Report the malaria status of this cell.
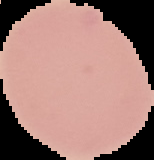

Uninfected.

{
  "preparation": "thin blood film",
  "image_size": "154×160 pixels",
  "image_type": "segmented cell region with the area outside set to black"
}